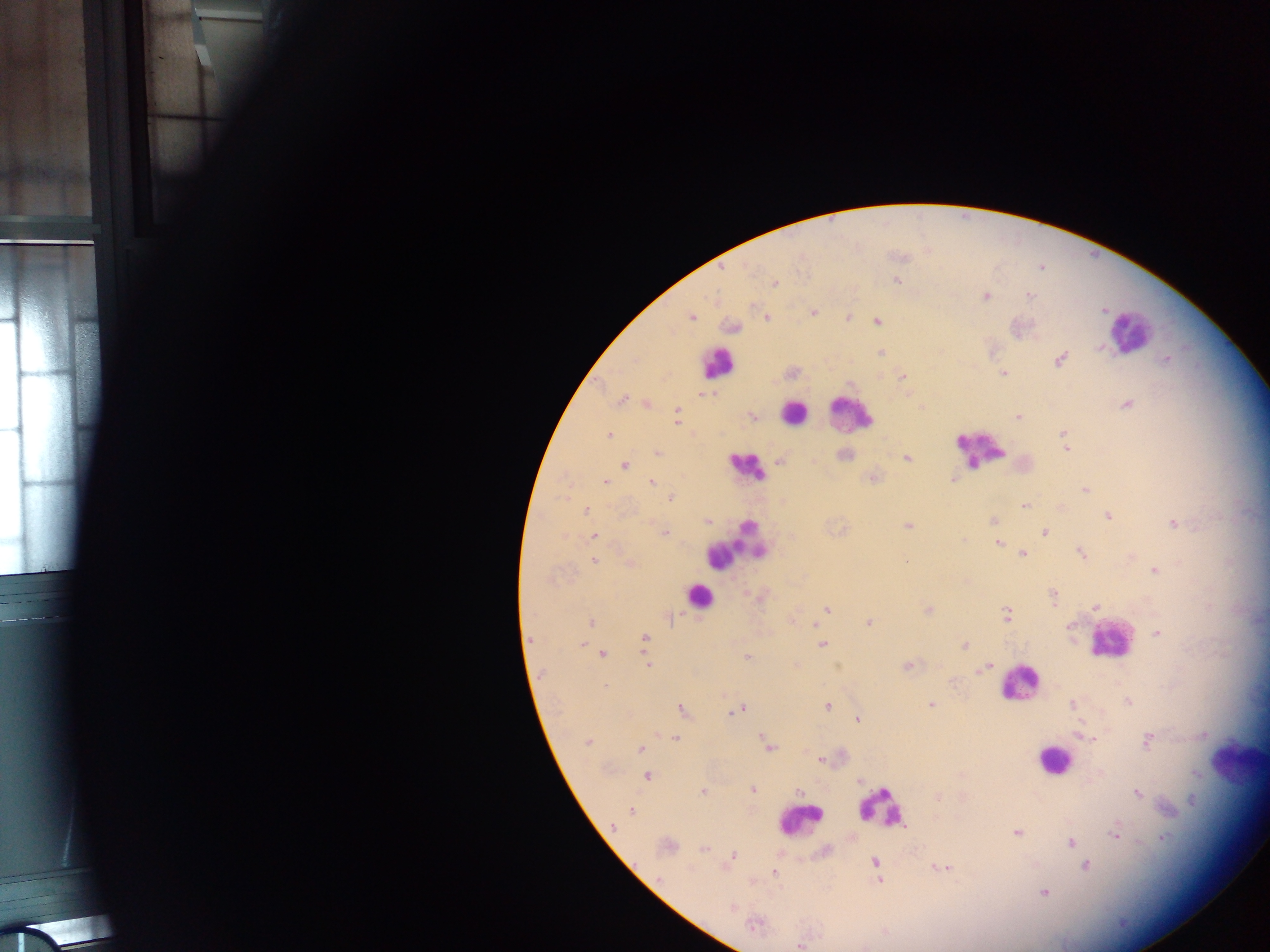

field of view = single
country = Ghana
Plasmodium parasite locations = approximate centers as x y in pixels: 897 281; 774 284; 1028 295; 986 296; 1104 310; 813 312; 691 317; 766 318; 877 322; 733 327; 1099 348; 882 353; 1060 359; 1167 359; 1003 373; 903 377; 701 394; 620 400; 1126 404; 647 405; 677 413; 751 416; 1019 417; 676 422; 1063 434; 608 435; 1065 446; 657 452; 907 458; 780 460; 624 465; 872 478; 953 479; 605 482; 651 483; 1085 490; 670 498; 1024 505; 586 510; 1108 516; 993 521; 708 523; 1174 524; 908 525; 665 532; 1044 532; 594 537; 998 543; 1023 554; 1081 554; 594 561; 630 564; 1155 571; 1053 597; 1095 607; 826 609; 928 610; 1006 614; 870 621; 591 622; 814 625; 1069 626; 1157 633; 645 638; 822 644; 581 645; 964 645; 603 653; 747 658; 647 664; 907 666; 986 666; 606 686; 1128 702; 931 704; 1072 704; 827 707; 681 710; 738 711; 858 719; 1084 736; 676 738; 765 739; 1147 741; 587 742; 769 746; 641 749; 821 760; 647 776; 753 790; 703 792; 800 792; 1138 793; 938 797; 1191 801; 631 811; 614 826; 1016 832; 1115 832; 1164 838; 1070 841; 704 849; 732 855; 876 861; 1085 866; 942 867; 774 872; 659 879; 878 880; 1044 893; 731 908; 755 924; 800 946
capture = mobile-phone photograph through a microscope
image size = 1270×952 pixels
preparation = thick blood film
leukocyte locations = approximate centers as x y in pixels: 1132 332; 717 363; 851 412; 793 413; 980 448; 745 467; 734 547; 698 596; 1109 641; 1019 682; 1053 760; 1236 760; 882 809; 799 822